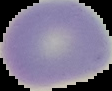

The area outside the segmented cell region is set to black. Malaria status: uninfected. Image is 112×91 pixels. From a thin blood film.